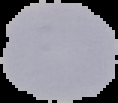
Image is 118×103 pixels. Result: no malaria parasites seen. From a thin blood film. The area outside the segmented cell region is set to black.